Outline each blood parasite and name the species.
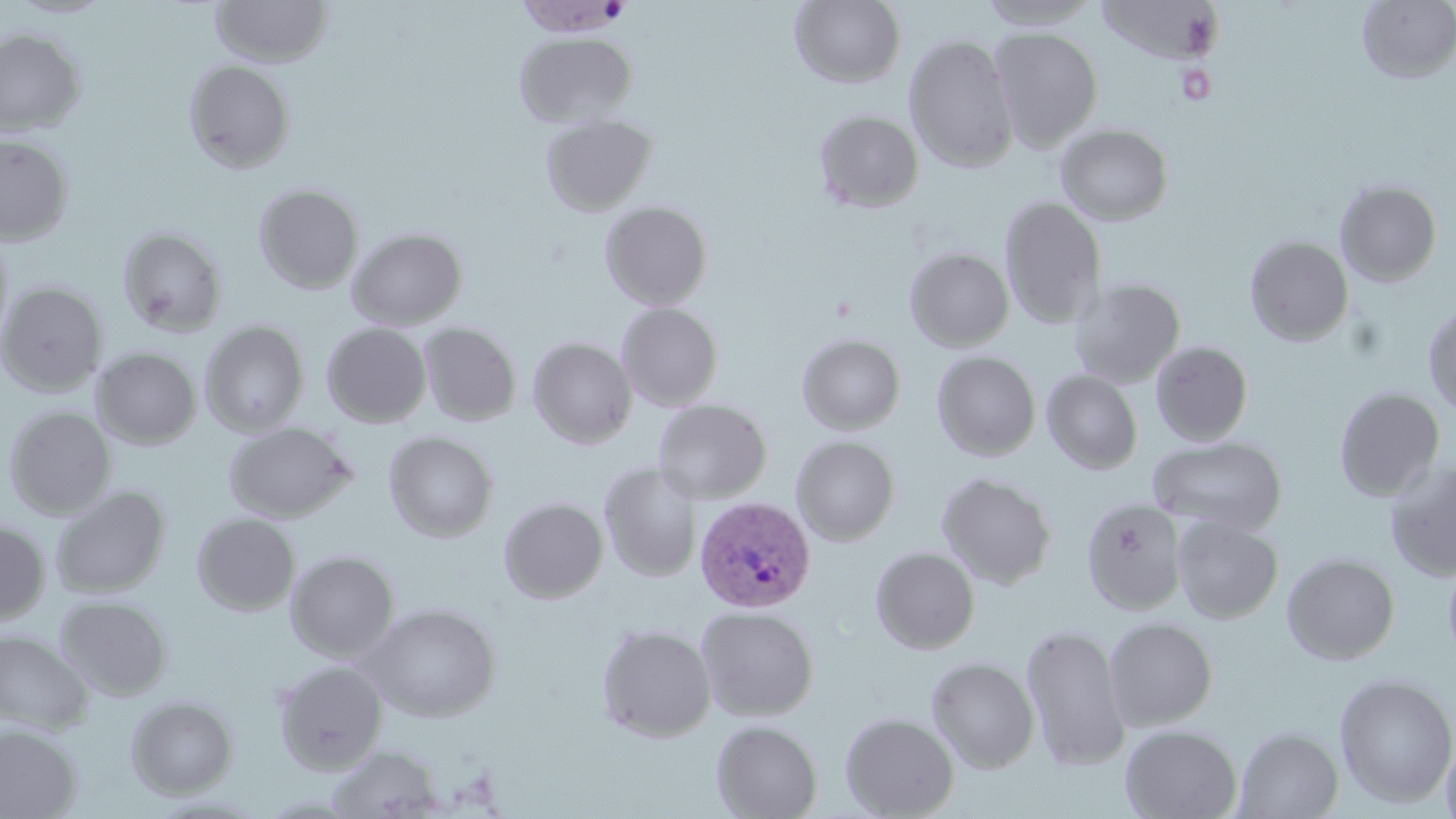

Approximate bounding boxes as (x1, y1, x2, y2) in pixels.
Plasmodium vivax-infected red blood cells: (695, 496, 816, 612).
No Plasmodium falciparum, Plasmodium ovale, Plasmodium malariae, Babesia divergens, or Trypanosoma brucei observed.

slide-level diagnosis = Plasmodium vivax
image size = 1456×819 pixels
platelet locations = approximate bounding boxes as (x1, y1, x2, y2) in pixels: (1176, 64, 1218, 104)
magnification = 1000x
uninfected red blood cell locations = approximate bounding boxes as (x1, y1, x2, y2) in pixels: (6, 0, 116, 18), (211, 0, 332, 67), (790, 0, 906, 88), (977, 0, 1102, 29), (1357, 1, 1456, 83), (988, 26, 1103, 152), (0, 29, 86, 136), (515, 33, 636, 128), (904, 34, 1019, 173), (184, 59, 296, 173), (813, 109, 923, 213), (540, 114, 657, 216), (1056, 124, 1173, 225), (0, 134, 74, 245), (1335, 180, 1442, 286), (254, 183, 364, 294), (999, 196, 1106, 329), (600, 201, 713, 310), (0, 227, 14, 351), (347, 227, 468, 330), (119, 228, 227, 337), (1245, 236, 1354, 346), (905, 247, 1014, 351), (1070, 277, 1185, 388), (0, 282, 108, 396), (617, 303, 723, 411), (1423, 304, 1456, 418), (200, 321, 309, 436), (322, 322, 432, 427), (419, 322, 521, 427), (796, 333, 906, 434), (528, 338, 637, 448), (1151, 341, 1253, 445), (91, 348, 201, 449), (932, 351, 1040, 460), (1042, 369, 1142, 474), (1334, 387, 1445, 502), (652, 399, 772, 504), (4, 406, 116, 518), (224, 422, 356, 522), (384, 431, 499, 542), (792, 436, 900, 545), (1148, 436, 1287, 536), (1385, 461, 1456, 581), (600, 462, 702, 582), (936, 471, 1057, 589), (51, 486, 170, 598), (499, 497, 608, 603), (1081, 498, 1187, 615), (192, 512, 300, 615), (1172, 516, 1283, 623), (0, 521, 50, 626), (871, 547, 979, 654), (286, 550, 399, 661), (1282, 553, 1400, 665), (1443, 557, 1456, 668), (55, 595, 173, 702), (361, 603, 502, 722), (696, 606, 819, 721), (1104, 618, 1217, 730), (1022, 623, 1131, 771), (598, 624, 716, 742), (0, 630, 94, 735), (926, 656, 1040, 773), (274, 660, 387, 773), (1334, 673, 1456, 807), (125, 696, 238, 798), (840, 712, 959, 818), (711, 720, 822, 819), (0, 723, 82, 819), (1120, 724, 1242, 818), (1234, 727, 1344, 818), (1440, 734, 1456, 819), (326, 745, 443, 818)
modality = light microscopy
stain = May-Grünwald-Giemsa
preparation = thin blood film
field of view = single